Comment on the morphology of the erythrocytes.
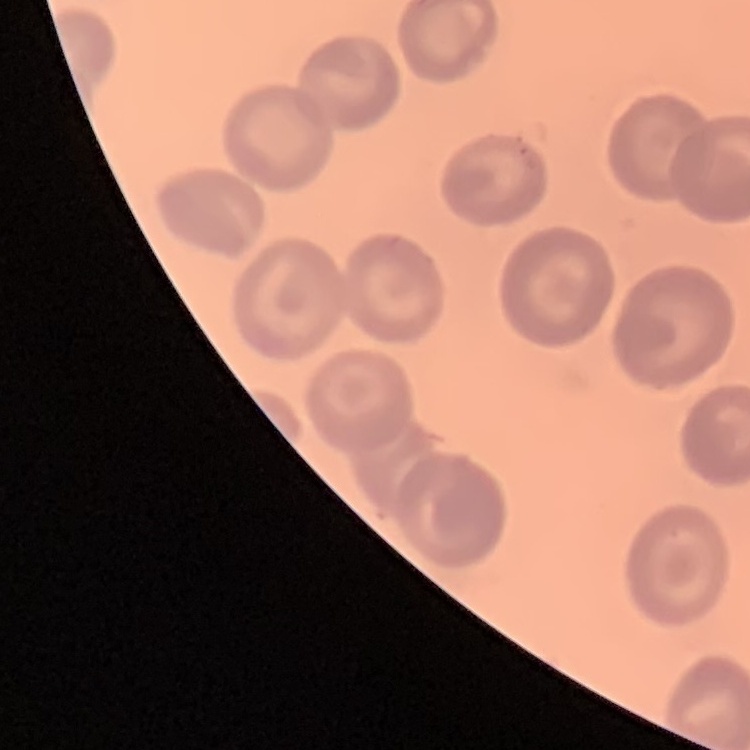
No rouleaux formation.

Thin blood film. One tile cut from a larger photomicrograph. Field's or Giemsa stain.